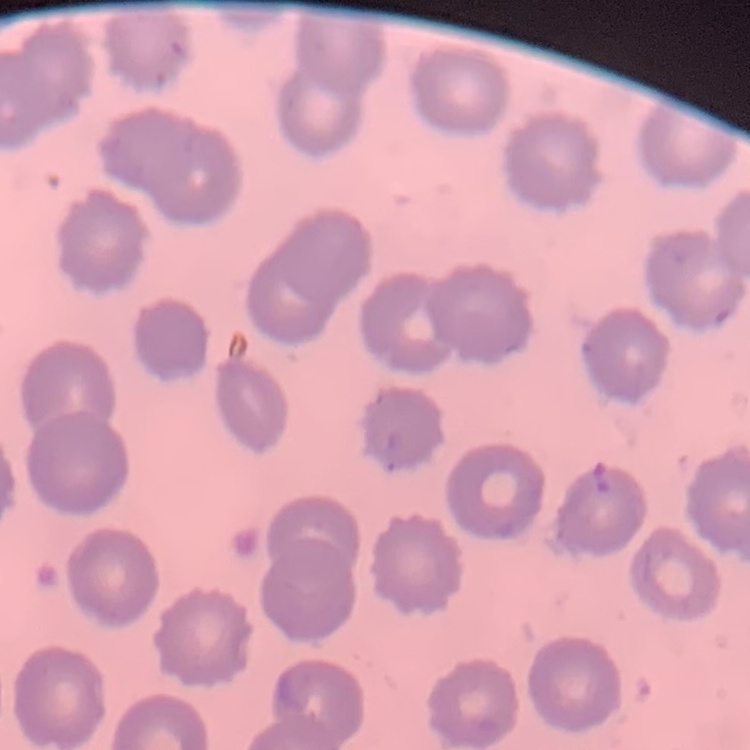 The erythrocytes exhibit no rouleaux formation. Stained with either Field's or Giemsa. One tile cut from a larger photomicrograph. Thin blood smear.